State the blood parasite species.
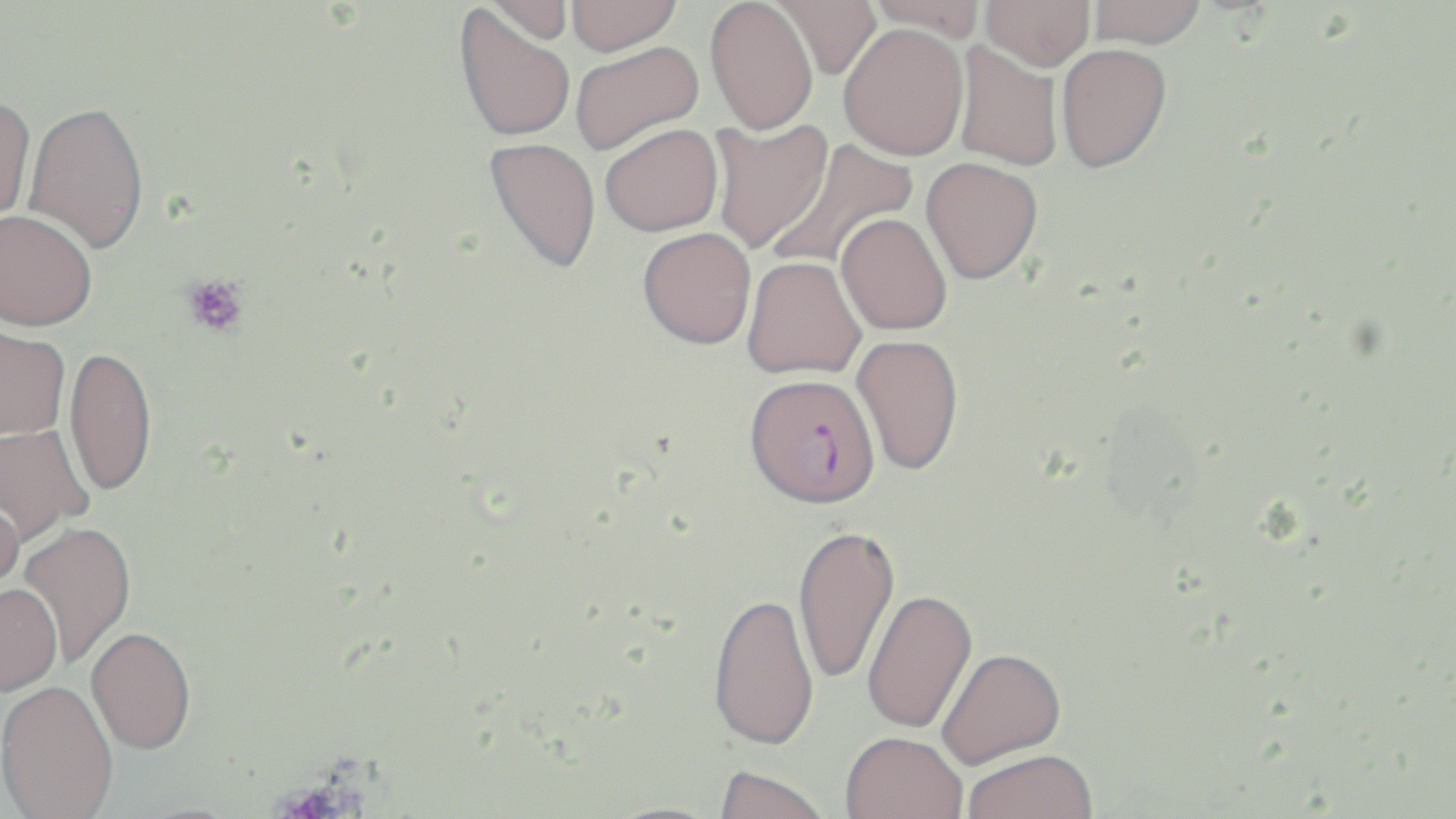

Plasmodium falciparum.

Approximate bounding boxes as (x1,y1)-(x2,y2) corner pairs in pixels. Platelet locations: (181,274)-(249,338). Uninfected red blood cell locations: (481,0)-(576,46), (565,0)-(682,55), (705,0)-(819,135), (768,0)-(881,79), (865,0)-(988,38), (980,0)-(1095,70), (1087,0)-(1206,49), (453,4)-(576,143), (838,23)-(968,160), (569,40)-(704,154), (953,41)-(1063,171), (1056,43)-(1171,172), (0,95)-(36,231), (23,102)-(149,254), (708,117)-(833,255), (599,123)-(723,236), (484,137)-(601,273), (767,137)-(918,273), (921,157)-(1044,284), (0,209)-(98,332), (836,212)-(952,335), (637,227)-(756,349), (742,255)-(866,379), (0,324)-(70,441), (851,334)-(964,476), (63,346)-(157,499), (0,423)-(94,545), (0,490)-(25,608), (18,523)-(137,667), (792,524)-(900,686), (1,586)-(62,698), (862,590)-(978,736), (708,593)-(819,755), (86,629)-(197,758), (936,648)-(1067,772), (0,682)-(118,819), (840,736)-(967,819), (962,753)-(1099,819), (713,769)-(831,819). Plasmodium falciparum-infected red blood cell locations: (744,373)-(880,509). Single field of view. Optical microscopy. Thin blood smear. Image is 1456×819 pixels. May-Grünwald-Giemsa stain. 1000x magnification.